Assess this cell for malaria.
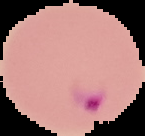

It is parasitized.

Segmented cell region on a black background. Image is 145×136 pixels. From a thin blood smear.